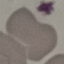

Summary:
  - Result: no malaria parasites detected
  - Capture: smartphone camera at the microscope eyepiece
  - Stain: Giemsa
  - Preparation: thin blood smear
  - Image type: automatically extracted cell patch, resized to 64 × 64 pixels